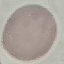
Summary:
  - Result: no malaria parasites seen
  - Image type: automatically extracted cell patch, resized to 64 × 64 pixels
  - Stain: Giemsa
  - Preparation: thin smear
  - Capture: smartphone camera at the microscope eyepiece